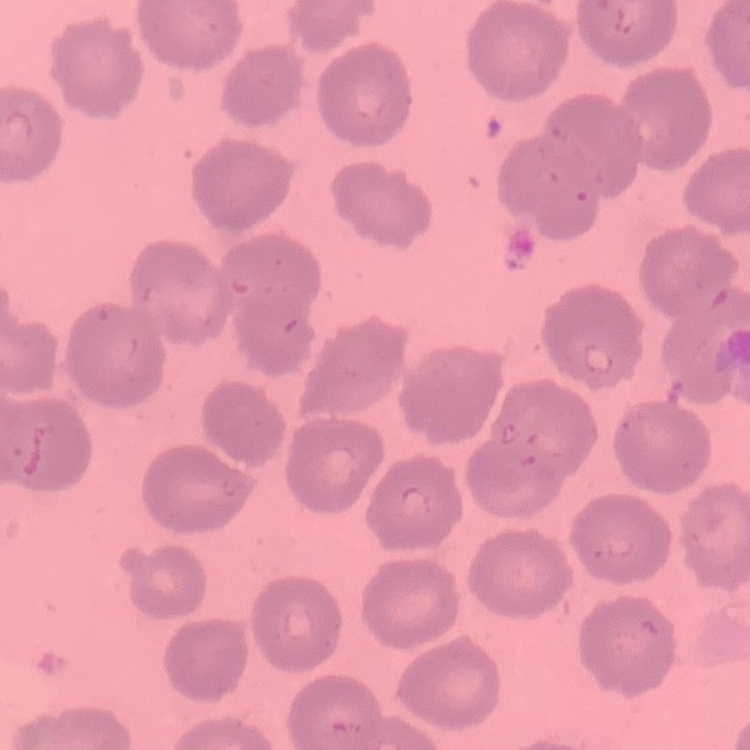

Summary:
  - Erythrocyte morphology: no rouleaux formation
  - Image type: one tile cut from a larger photomicrograph
  - Stain: Field's or Giemsa
  - Preparation: thin blood film